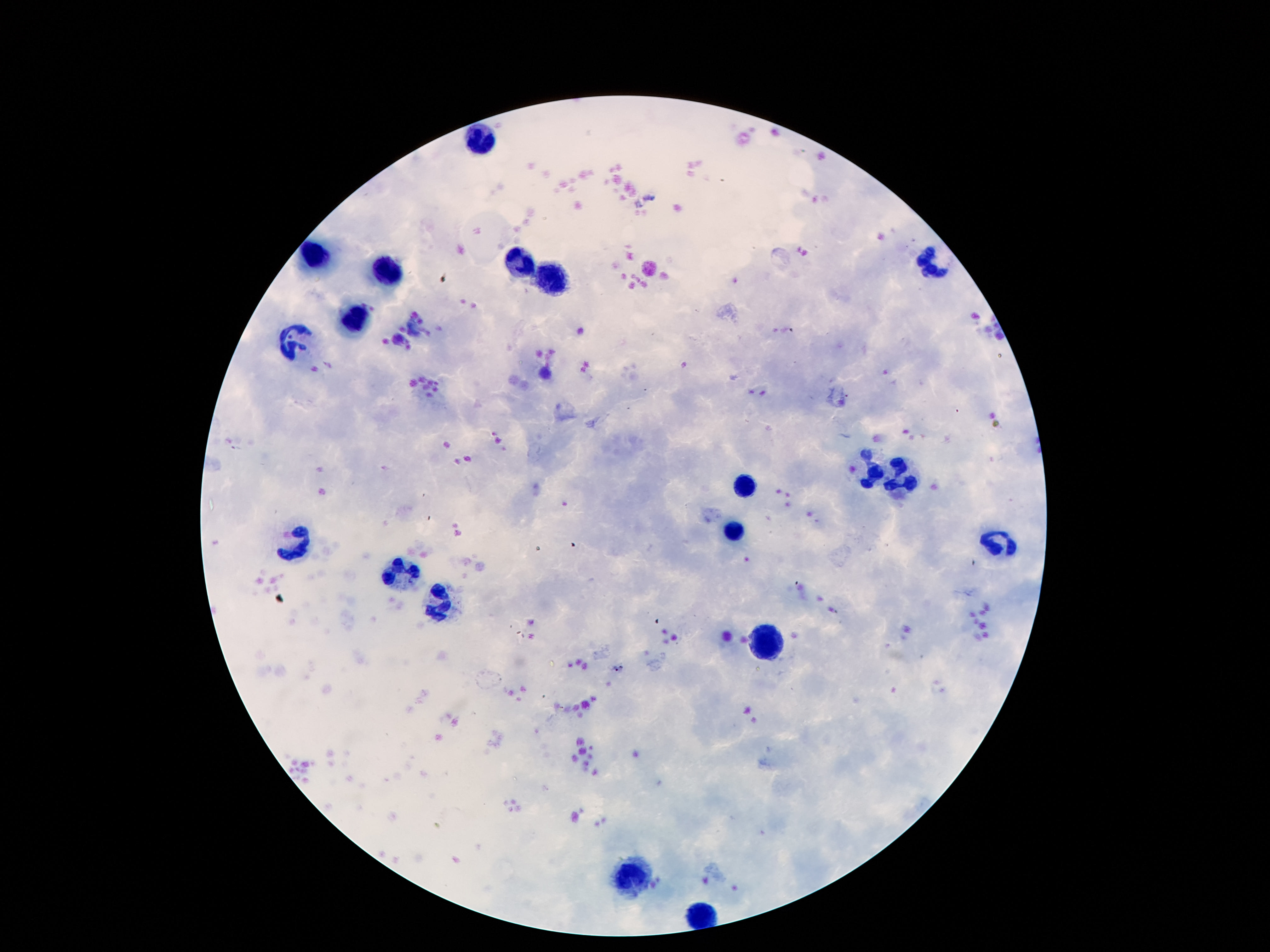
patient_malaria_status: negative
magnification: 100x
capture: smartphone camera through the microscope eyepiece
image_size: 1270×952 pixels
field_of_view: single
preparation: thick blood film
leukocyte_locations: 'approximate centers as {x, y} in pixels: {480, 136}, {312, 255}, {516, 262}, {928, 262}, {388, 273}, {552, 278}, {354, 323}, {300, 341}, {873, 474}, {904, 476}, {745, 486}, {732, 529}, {997, 543}, {298, 544}, {400, 577}, {440, 602}, {768, 639}, {627, 879}, {703, 917}'
stain: Giemsa